Classify this cell by malaria status.
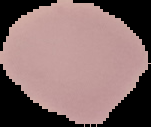

Uninfected.

Summary:
  - Image size: 151×127 pixels
  - Image type: segmented cell region with the area outside set to black
  - Preparation: thin blood film